Identify the parasite.
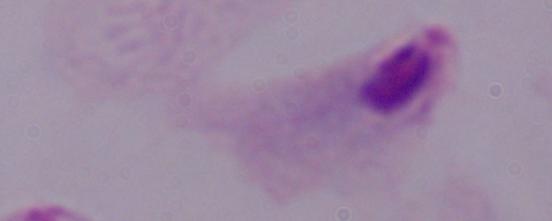

A trichomonad.

Summary:
  - Magnification: 1000x
  - Modality: micrograph